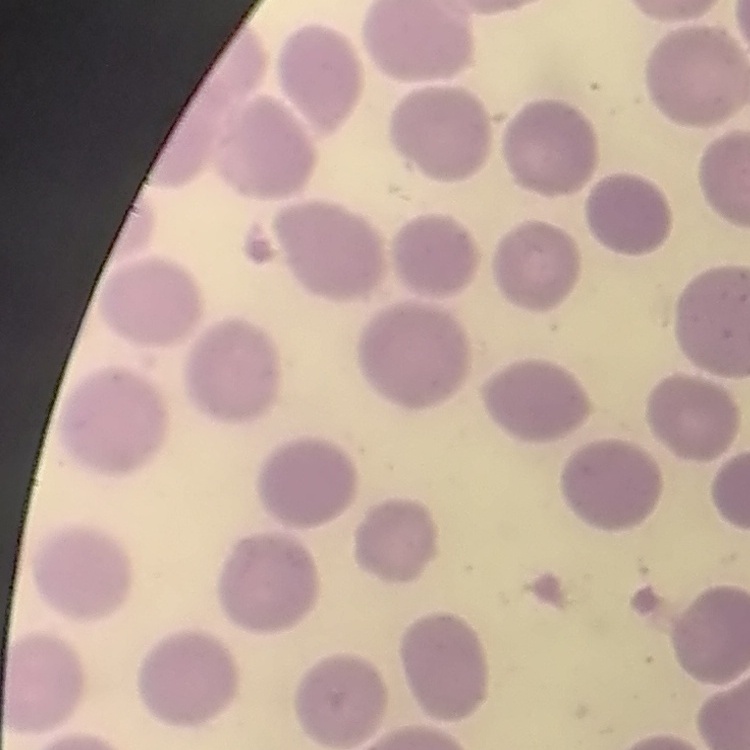
Summary:
  - Erythrocyte morphology: no rouleaux formation
  - Stain: Field's or Giemsa
  - Image type: one tile cut from a larger photomicrograph
  - Preparation: thin blood film